Report the malaria status of this cell.
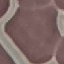

Uninfected.

Automatically extracted cell patch, resized to 64 × 64 pixels. Thin blood smear. Giemsa stain. Photographed with a smartphone camera at the microscope eyepiece.